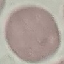

{
  "result": "no malaria parasites seen",
  "capture": "smartphone camera at the microscope eyepiece",
  "stain": "Giemsa",
  "preparation": "thin blood smear",
  "image_type": "cell patch, automatically extracted from a larger field of view and resized to 64 × 64 pixels"
}